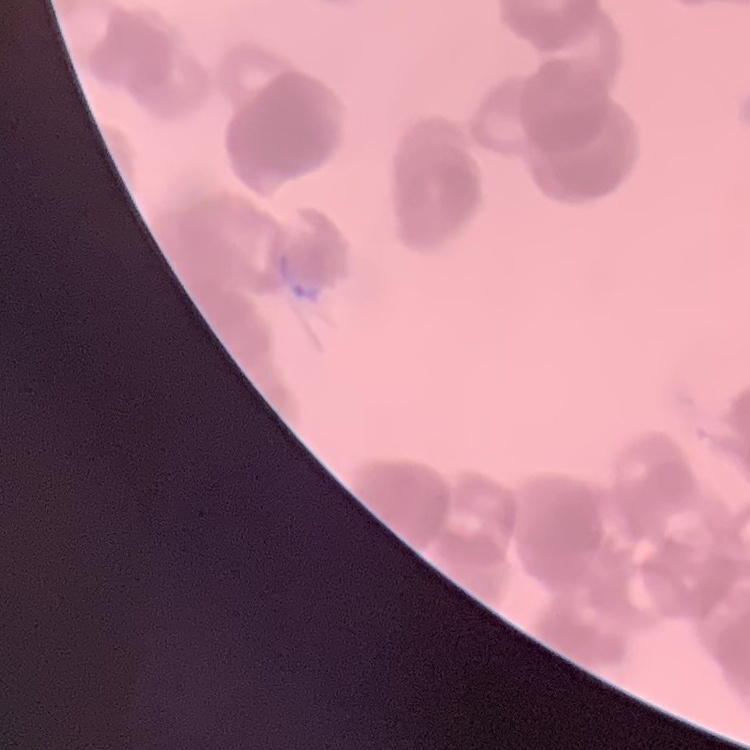
The erythrocytes exhibit rouleaux formation. Stained with either Field's or Giemsa. Thin blood film. One tile cut from a larger photomicrograph.